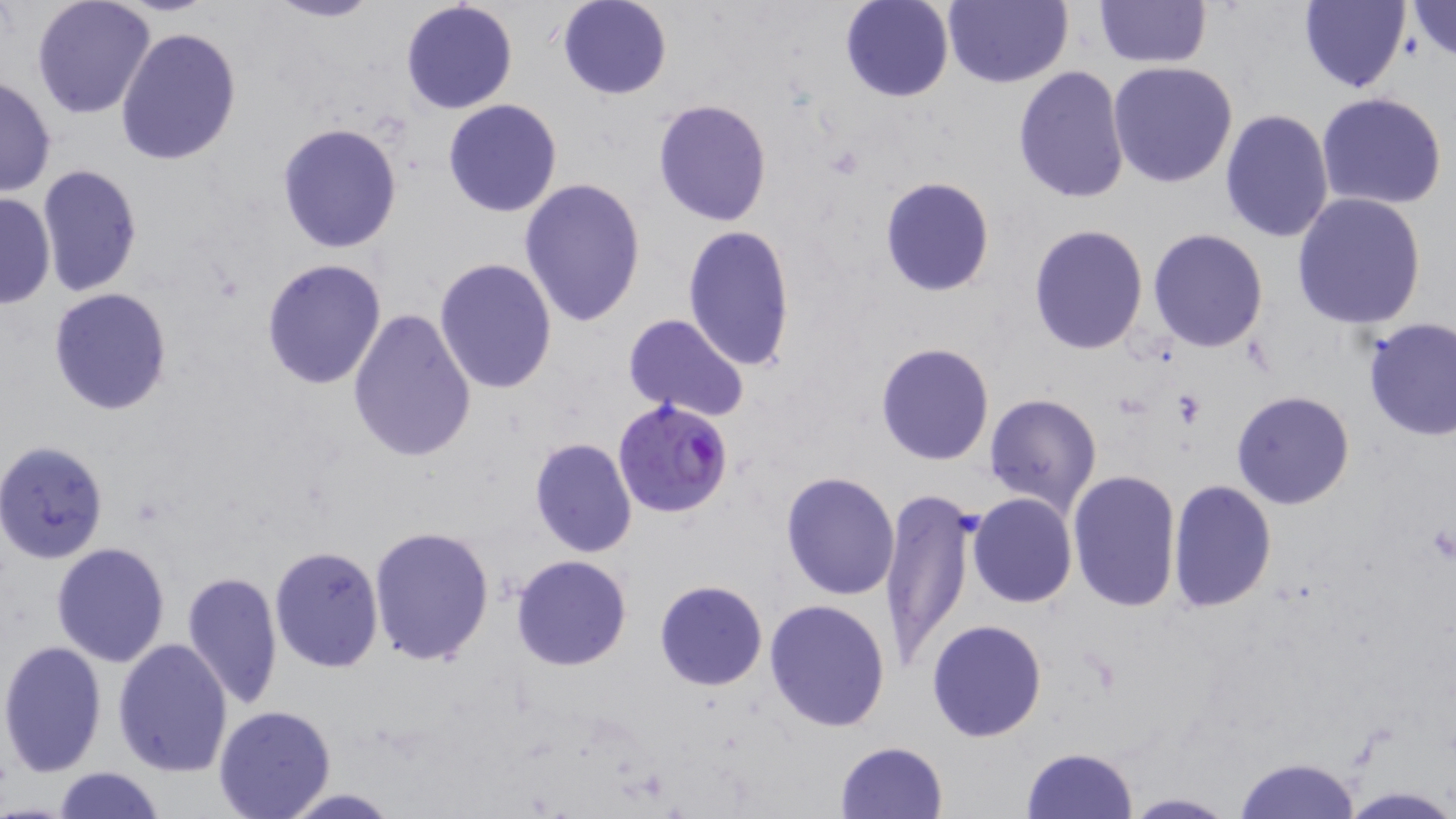
Summary:
  - Coordinate format: approximate bounding boxes as (x1, y1, x2, y2) in pixels
  - Uninfected red blood cell locations: (31, 0, 157, 120), (261, 0, 384, 24), (943, 0, 1072, 88), (399, 1, 520, 115), (557, 1, 672, 100), (840, 1, 954, 103), (1094, 1, 1213, 69), (1298, 1, 1410, 93), (1403, 2, 1456, 64), (114, 25, 240, 166), (1108, 62, 1239, 188), (1012, 67, 1130, 204), (1, 75, 58, 198), (1316, 92, 1448, 210), (652, 98, 774, 227), (443, 100, 563, 219), (1219, 108, 1335, 243), (277, 122, 403, 253), (37, 164, 142, 296), (878, 176, 995, 296), (518, 179, 647, 328), (0, 191, 55, 310), (1289, 192, 1428, 329), (1028, 223, 1147, 357), (681, 224, 796, 370), (1148, 229, 1269, 352), (260, 257, 388, 392), (434, 257, 559, 395), (48, 287, 174, 415), (348, 307, 477, 462), (621, 313, 749, 423), (1361, 317, 1455, 442), (874, 342, 995, 467), (1231, 391, 1355, 510), (983, 393, 1102, 517), (528, 437, 638, 557), (0, 440, 109, 563), (1066, 469, 1182, 613), (781, 470, 901, 601), (1168, 479, 1278, 614), (879, 488, 977, 664), (968, 493, 1078, 608), (368, 526, 496, 667), (51, 542, 170, 666), (269, 545, 384, 673), (511, 554, 633, 671), (180, 570, 284, 710), (653, 579, 769, 691), (764, 599, 892, 733), (926, 619, 1048, 742), (0, 639, 108, 778), (113, 639, 233, 778), (213, 705, 338, 819), (833, 740, 948, 819), (1023, 746, 1138, 818), (1231, 757, 1363, 818), (51, 766, 165, 819), (1336, 786, 1456, 818), (275, 788, 407, 818), (1118, 792, 1238, 818)
  - Platelet locations: (1171, 391, 1205, 426)
  - Plasmodium falciparum-infected red blood cell locations: (612, 398, 733, 521)
  - Slide-level diagnosis: Plasmodium falciparum
  - Modality: light microscopy
  - Stain: May-Grünwald-Giemsa
  - Field of view: single
  - Image size: 1456×819 pixels
  - Magnification: 1000x
  - Preparation: thin blood smear